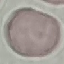

malaria_status: uninfected
preparation: thin blood smear
image_type: cell patch, automatically extracted from a larger field of view and resized to 64 × 64 pixels
capture: smartphone camera at the microscope eyepiece
stain: Giemsa